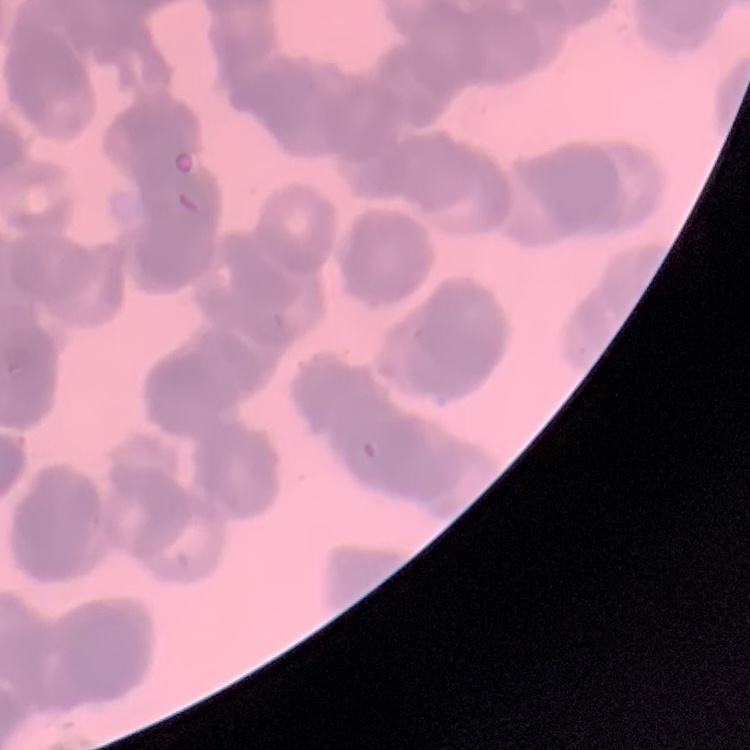
erythrocyte morphology = rouleaux formation
stain = Field's or Giemsa
preparation = thin blood smear
image type = square crop of a larger photomicrograph